Assess this cell for malaria.
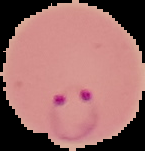

Parasitized.

From a thin blood smear. Image is 145×151 pixels. Segmented cell region on a black background.